Locate every Plasmodium vivax-infected red blood cell.
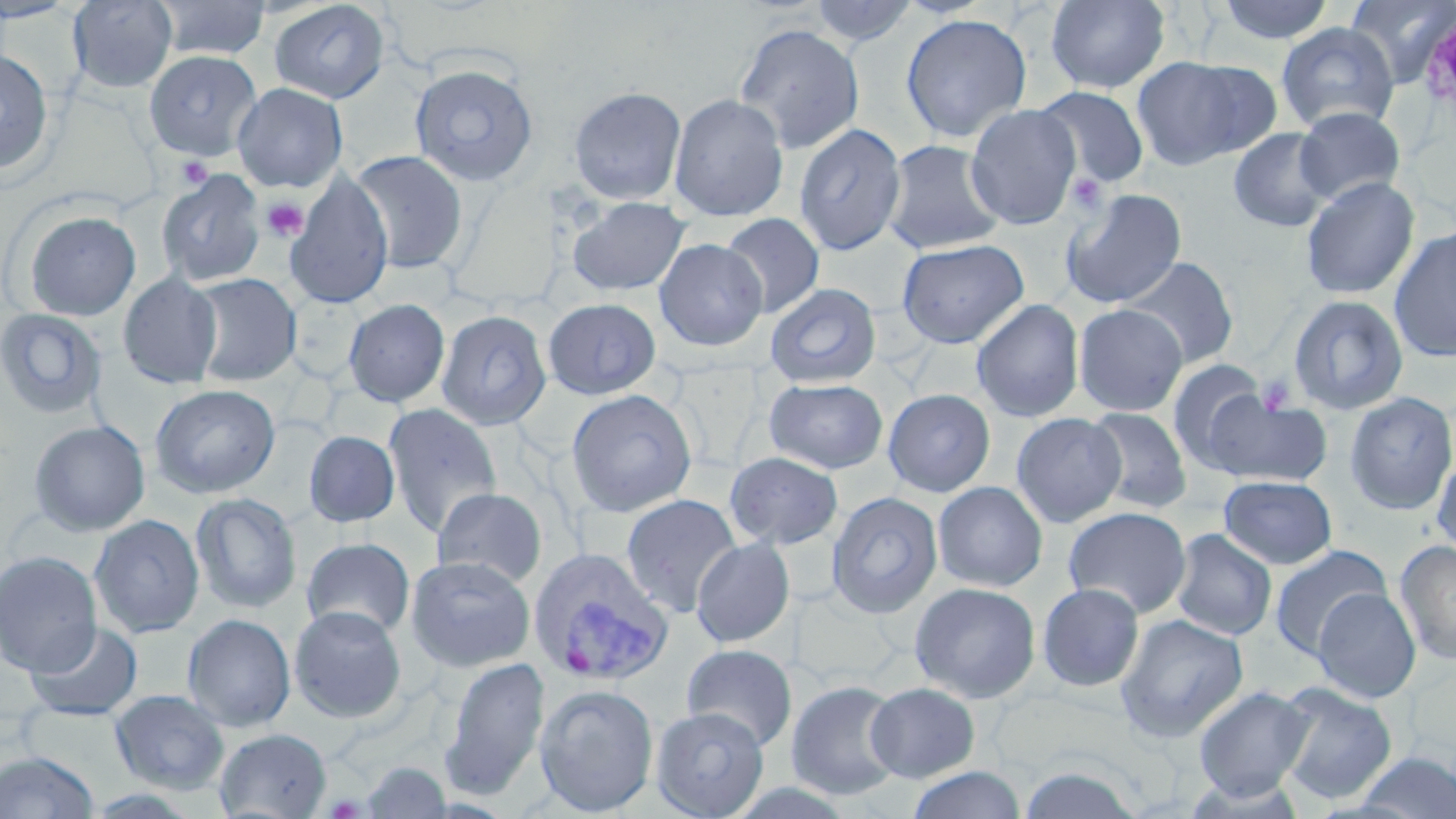
Approximate bounding boxes as named x1/y1/x2/y2 corners in pixels.
Plasmodium vivax-infected red blood cells: (x1=529, y1=547, x2=672, y2=686).

Summary:
  - Platelet locations: (x1=176, y1=156, x2=213, y2=190), (x1=1068, y1=173, x2=1108, y2=217), (x1=261, y1=197, x2=308, y2=241), (x1=325, y1=795, x2=365, y2=818)
  - Uninfected red blood cell locations: (x1=67, y1=0, x2=178, y2=93), (x1=151, y1=0, x2=271, y2=61), (x1=808, y1=0, x2=920, y2=48), (x1=1045, y1=0, x2=1170, y2=95), (x1=1212, y1=0, x2=1337, y2=44), (x1=1345, y1=0, x2=1456, y2=87), (x1=0, y1=1, x2=81, y2=23), (x1=268, y1=1, x2=391, y2=104), (x1=900, y1=13, x2=1032, y2=143), (x1=733, y1=22, x2=865, y2=154), (x1=1275, y1=22, x2=1399, y2=134), (x1=0, y1=46, x2=55, y2=176), (x1=143, y1=50, x2=263, y2=161), (x1=1131, y1=55, x2=1276, y2=171), (x1=409, y1=63, x2=540, y2=187), (x1=232, y1=82, x2=348, y2=193), (x1=568, y1=85, x2=687, y2=205), (x1=1032, y1=86, x2=1150, y2=189), (x1=669, y1=94, x2=789, y2=222), (x1=965, y1=104, x2=1083, y2=231), (x1=1293, y1=106, x2=1406, y2=205), (x1=793, y1=122, x2=907, y2=256), (x1=1228, y1=128, x2=1335, y2=232), (x1=882, y1=139, x2=1007, y2=254), (x1=349, y1=150, x2=468, y2=274), (x1=156, y1=169, x2=267, y2=287), (x1=284, y1=173, x2=393, y2=309), (x1=1299, y1=176, x2=1420, y2=299), (x1=1061, y1=187, x2=1188, y2=308), (x1=566, y1=196, x2=691, y2=296), (x1=21, y1=209, x2=142, y2=321), (x1=720, y1=212, x2=825, y2=319), (x1=1388, y1=225, x2=1456, y2=364), (x1=654, y1=238, x2=768, y2=351), (x1=897, y1=238, x2=1029, y2=349), (x1=1119, y1=256, x2=1239, y2=369), (x1=188, y1=272, x2=301, y2=387), (x1=118, y1=273, x2=222, y2=389), (x1=764, y1=282, x2=882, y2=388), (x1=1287, y1=293, x2=1409, y2=415), (x1=343, y1=298, x2=450, y2=407), (x1=542, y1=298, x2=661, y2=400), (x1=971, y1=298, x2=1085, y2=423), (x1=1074, y1=303, x2=1188, y2=416), (x1=0, y1=308, x2=108, y2=419), (x1=436, y1=309, x2=552, y2=430), (x1=1167, y1=359, x2=1271, y2=468), (x1=764, y1=378, x2=889, y2=474), (x1=149, y1=384, x2=281, y2=499), (x1=883, y1=388, x2=995, y2=497), (x1=565, y1=389, x2=698, y2=518), (x1=1204, y1=390, x2=1332, y2=488), (x1=1343, y1=392, x2=1456, y2=516), (x1=383, y1=402, x2=502, y2=538), (x1=1085, y1=407, x2=1192, y2=514), (x1=1011, y1=412, x2=1126, y2=527), (x1=29, y1=420, x2=151, y2=537), (x1=304, y1=430, x2=400, y2=528), (x1=306, y1=431, x2=404, y2=638), (x1=1432, y1=450, x2=1456, y2=560), (x1=723, y1=451, x2=844, y2=551), (x1=1218, y1=475, x2=1338, y2=570), (x1=932, y1=481, x2=1048, y2=592), (x1=432, y1=486, x2=547, y2=588), (x1=827, y1=491, x2=943, y2=618), (x1=190, y1=493, x2=303, y2=614), (x1=620, y1=493, x2=742, y2=617), (x1=1063, y1=506, x2=1191, y2=619), (x1=89, y1=514, x2=204, y2=639), (x1=1170, y1=529, x2=1277, y2=641), (x1=691, y1=537, x2=796, y2=648), (x1=302, y1=538, x2=415, y2=639), (x1=1394, y1=540, x2=1456, y2=667), (x1=1269, y1=545, x2=1391, y2=660), (x1=0, y1=550, x2=103, y2=676), (x1=405, y1=555, x2=536, y2=672), (x1=909, y1=582, x2=1041, y2=703), (x1=1036, y1=582, x2=1145, y2=692), (x1=1312, y1=586, x2=1421, y2=704), (x1=289, y1=605, x2=408, y2=723), (x1=182, y1=613, x2=296, y2=732), (x1=1115, y1=614, x2=1249, y2=743), (x1=25, y1=622, x2=143, y2=722), (x1=681, y1=643, x2=798, y2=751), (x1=440, y1=656, x2=551, y2=799), (x1=785, y1=679, x2=904, y2=801), (x1=1274, y1=680, x2=1398, y2=804), (x1=865, y1=681, x2=980, y2=782), (x1=533, y1=682, x2=659, y2=816), (x1=1193, y1=685, x2=1313, y2=799), (x1=109, y1=689, x2=231, y2=794), (x1=651, y1=706, x2=769, y2=819), (x1=214, y1=727, x2=332, y2=818), (x1=0, y1=750, x2=99, y2=818), (x1=1352, y1=751, x2=1456, y2=818), (x1=357, y1=763, x2=457, y2=818), (x1=1017, y1=764, x2=1143, y2=819), (x1=906, y1=766, x2=1027, y2=819), (x1=1180, y1=773, x2=1309, y2=818)
  - Slide-level diagnosis: Plasmodium vivax
  - Modality: light microscopy
  - Magnification: 1000x
  - Image size: 1456×819 pixels
  - Stain: May-Grünwald-Giemsa
  - Preparation: thin blood smear
  - Field of view: single